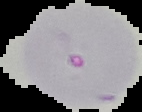

result = malaria parasites identified
preparation = thin blood smear
image size = 142×112 pixels
image type = segmented cell region with the area outside set to black